Evaluate for malaria.
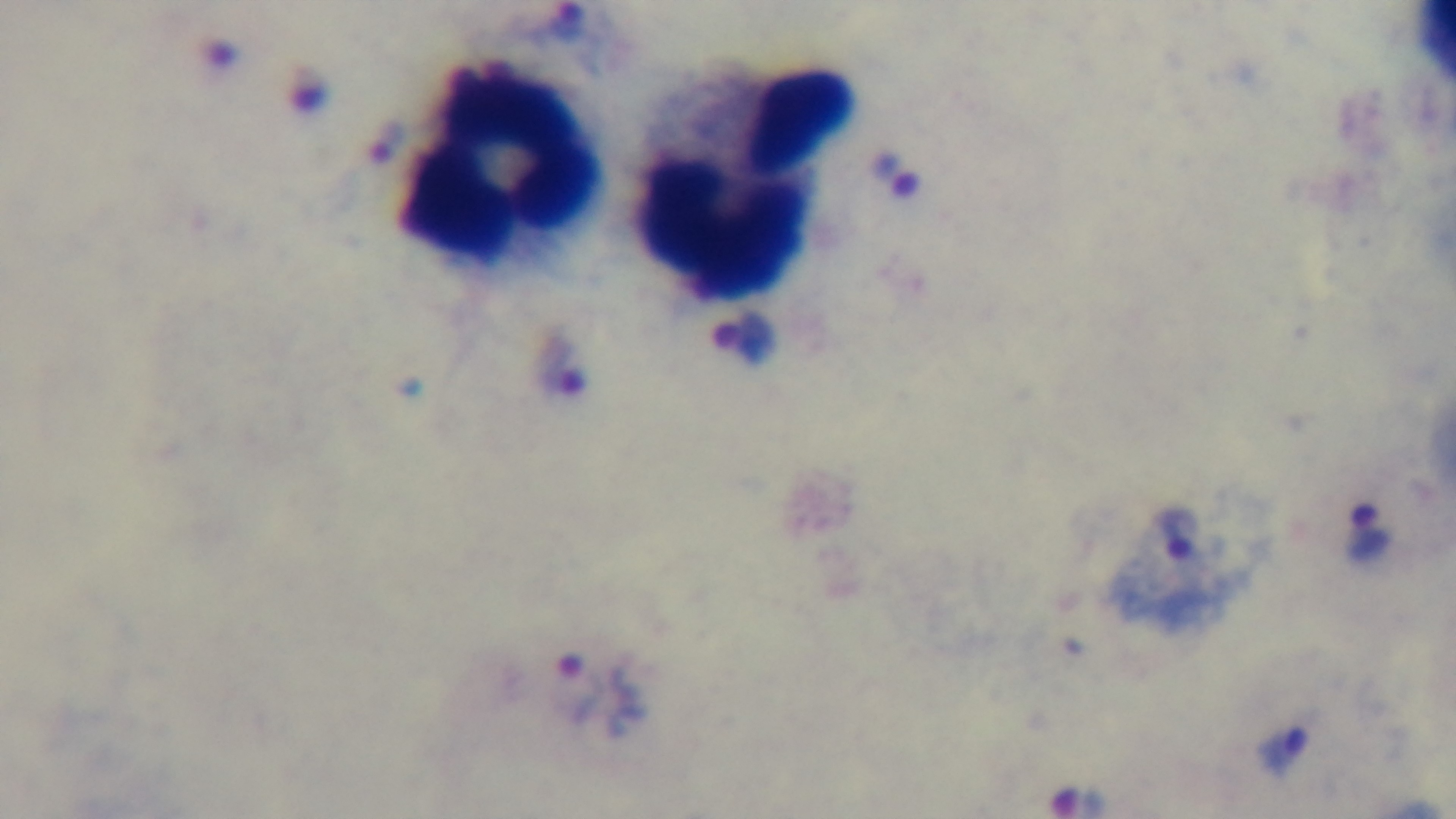

It is infected.

Summary:
  - Preparation: thick
  - Field of view: single
  - Stain: Giemsa
  - Modality: light microscopy
  - Capture: mounted 4K digital camera
  - Objective: 100x oil immersion